Give the position of every Plasmodium parasite.
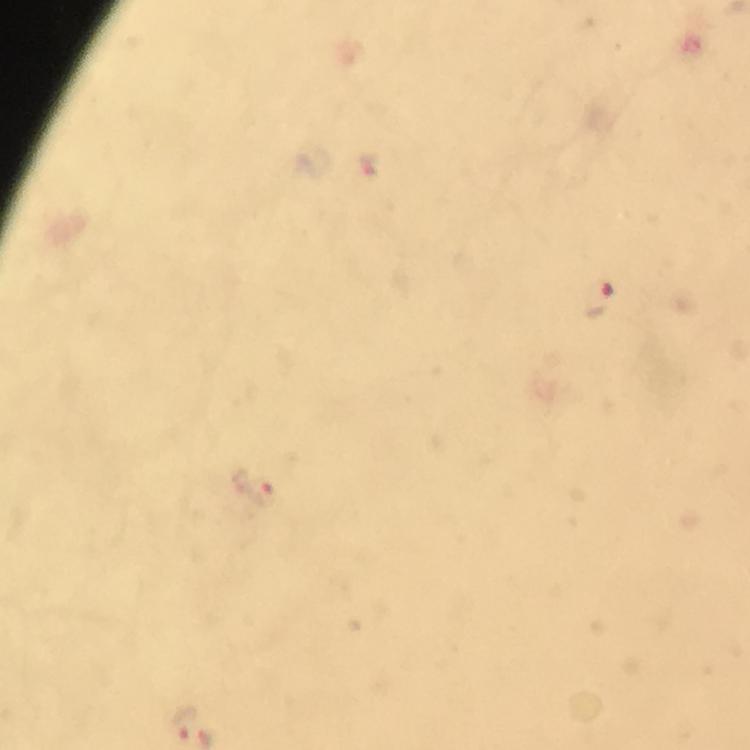
Approximate centers as {x, y} in pixels.
Plasmodium parasites: {368, 167}, {599, 300}, {254, 485}.

Immersion oil was used. Photographed through the microscope with a smartphone camera. 100x magnification. From a malaria diagnostic workup. Image is 750×750 pixels. A crop from one field of view. Giemsa stain. Thick blood smear.